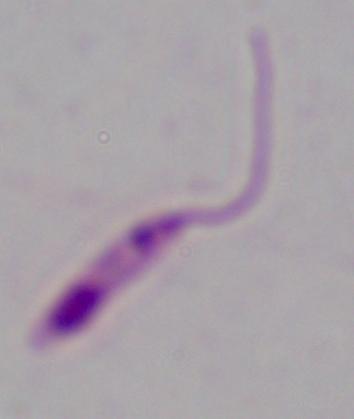

1000x magnification. Micrograph. A Leishmania parasite is seen.